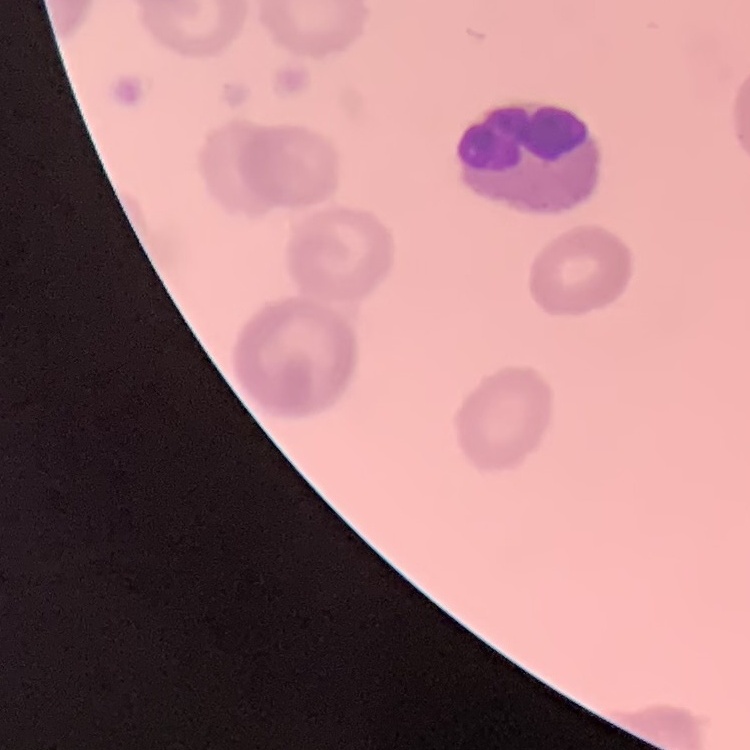

erythrocyte morphology = rouleaux formation
preparation = thin blood smear
image type = square crop of a larger photomicrograph
stain = Field's or Giemsa